Assess this cell for malaria.
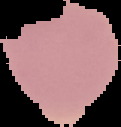
Uninfected.

The area outside the segmented cell region is set to black. Image is 121×127 pixels. From a thin blood film.